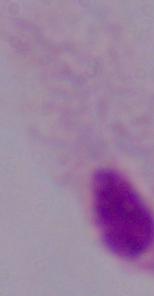 1000x magnification. Micrograph. A trichomonad is seen.